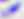

magnification = 400x
modality = photomicrograph
identification = Toxoplasma gondii